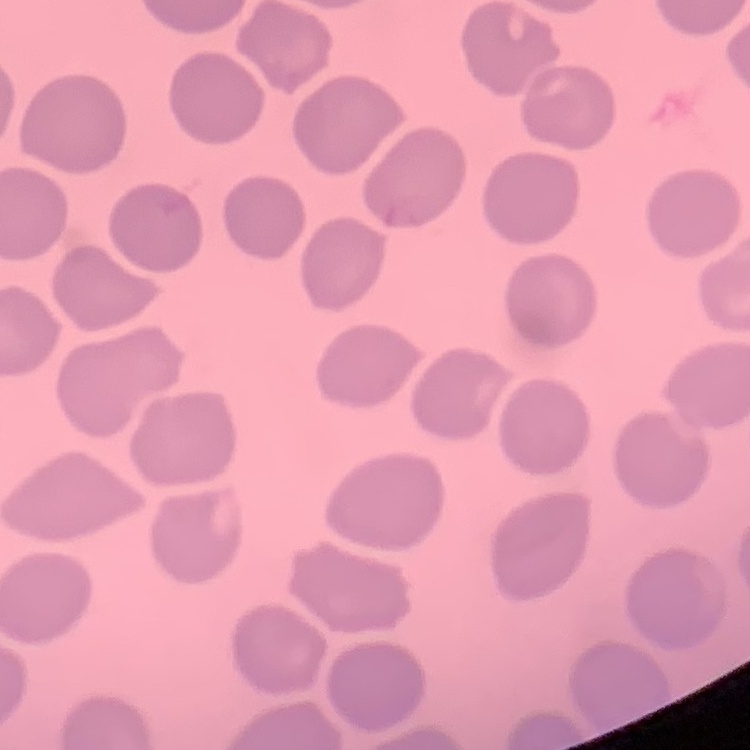
erythrocyte morphology = no rouleaux formation
image type = one tile cut from a larger photomicrograph
stain = Field's or Giemsa
preparation = thin peripheral smear